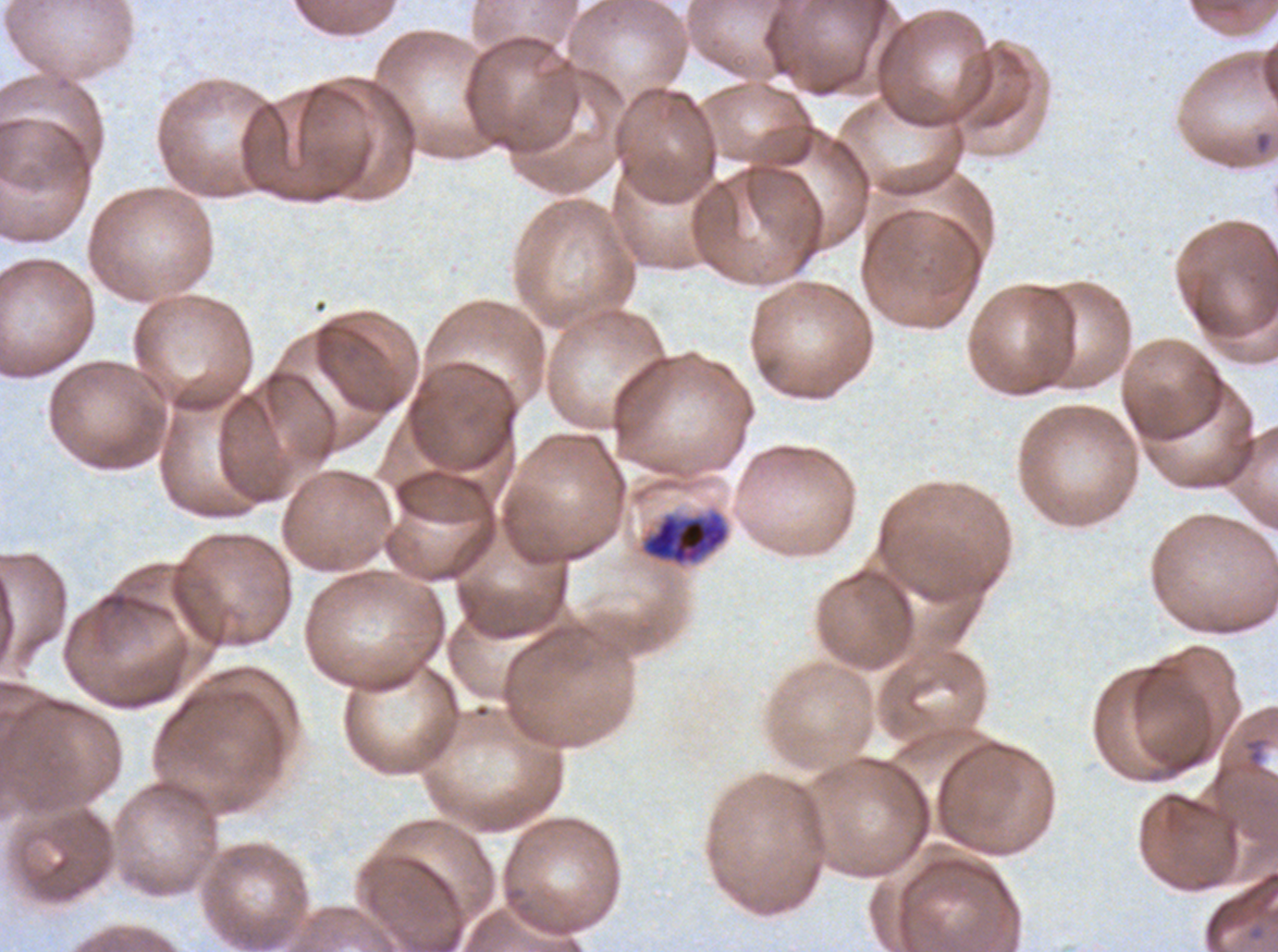
Approximate bounding boxes as {x1, y1, x2, y2} in pixels. Early schizont locations: {639, 508, 731, 568}. Thin blood smear. Giemsa stain. One sub-image of a larger composite. Plasmodium falciparum from a patient in The Gambia, cultured ex vivo for 24 to 48 hours. Image is 1278×952 pixels.